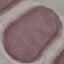
Summary:
  - Malaria status: uninfected
  - Preparation: thin smear
  - Stain: Giemsa
  - Image type: cell patch, automatically extracted from a larger field of view and resized to 64 × 64 pixels
  - Capture: smartphone through the microscope eyepiece